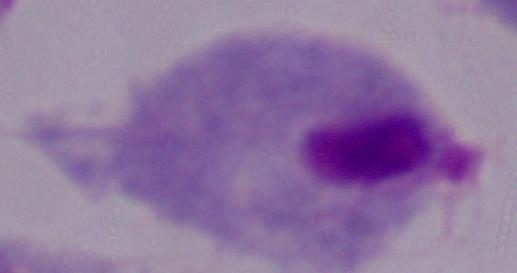

Photomicrograph. Captured at 1000x magnification. A trichomonad is seen.